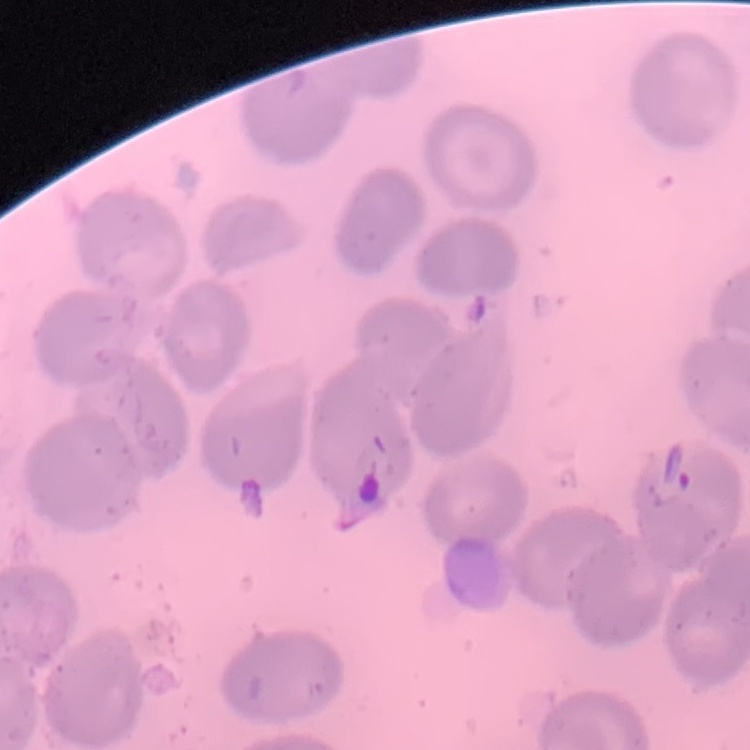

Summary:
  - Erythrocyte morphology: no rouleaux formation
  - Image type: square crop of a larger photomicrograph
  - Preparation: thin blood film
  - Stain: Field's or Giemsa